Describe the morphology of the erythrocytes.
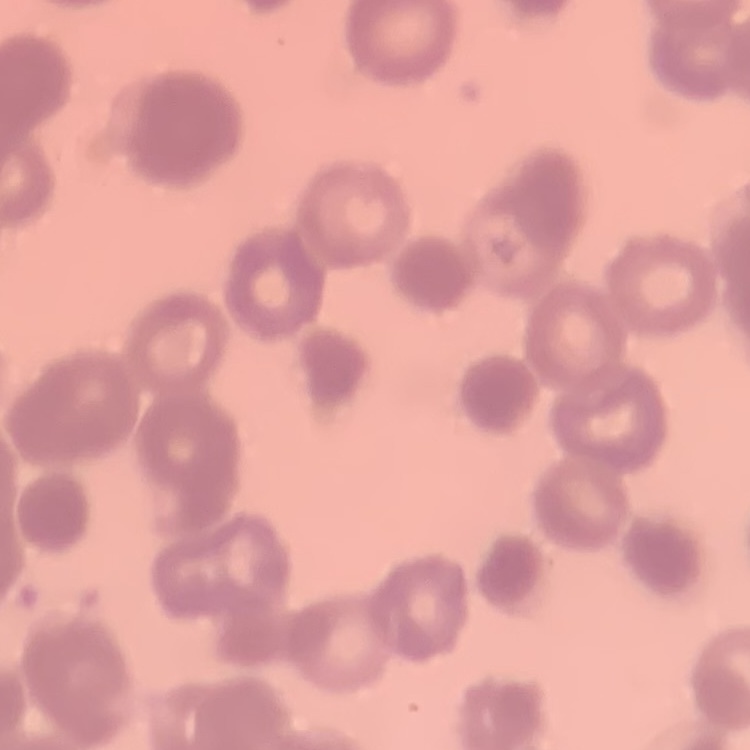

Rouleaux formation.

Stained with either Field's or Giemsa. One tile cut from a larger photomicrograph. Thin blood smear.